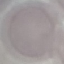 Malaria status: uninfected. Giemsa-stained preparation. Thin smear of blood. Photographed with a smartphone camera at the microscope eyepiece. Cell patch, automatically extracted from a larger field of view and resized to 64 × 64 pixels.